Report the malaria status of this cell.
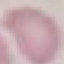

It is uninfected.

image type = cell patch, automatically extracted from a larger field of view and resized to 64 × 64 pixels
capture = smartphone camera at the microscope eyepiece
preparation = thin smear
stain = Giemsa